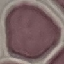

Summary:
  - Result: no malaria parasites seen
  - Capture: smartphone through the microscope eyepiece
  - Stain: Giemsa
  - Image type: cell patch, automatically extracted from a larger field of view and resized to 64 × 64 pixels
  - Preparation: thin blood smear